Locate every blood parasite and identify its species.
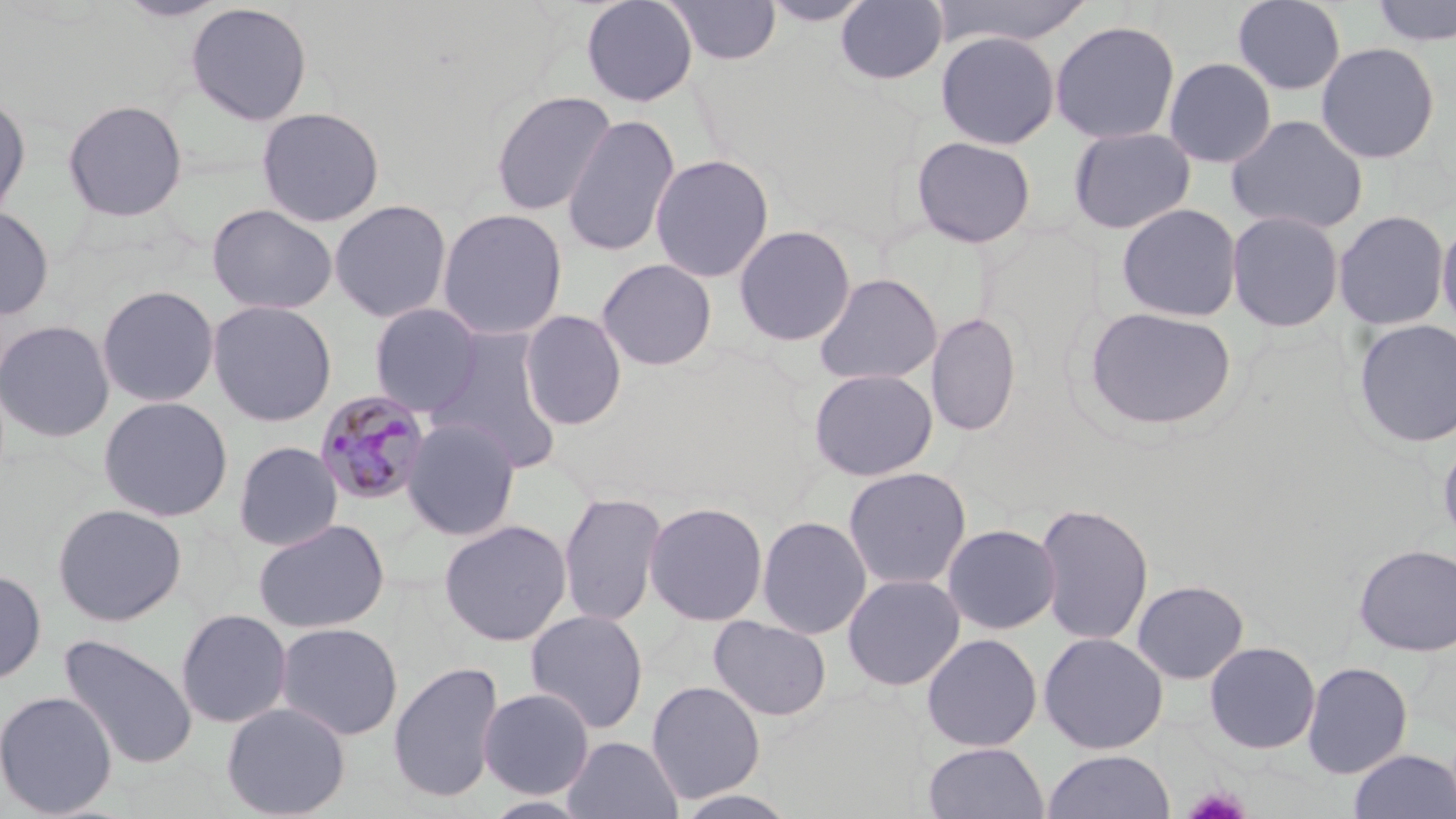

Approximate bounding boxes as [x1, y1, x2, y2] in pixels.
Plasmodium malariae-infected red blood cells: [314, 389, 432, 508].
No Plasmodium falciparum, Plasmodium ovale, Plasmodium vivax, Babesia divergens, or Trypanosoma brucei observed.

slide_level_diagnosis: Plasmodium malariae
field_of_view: single
stain: May-Grünwald-Giemsa
modality: light microscopy
magnification: 1000x
platelet_locations: 'approximate bounding boxes as [x1, y1, x2, y2] in pixels: [1181, 786, 1252, 818]'
preparation: thin blood smear
uninfected_red_blood_cell_locations: 'approximate bounding boxes as [x1, y1, x2, y2] in pixels: [117, 0, 230, 23], [580, 0, 699, 107], [664, 0, 782, 65], [760, 0, 874, 27], [835, 0, 948, 86], [929, 0, 1094, 48], [1231, 0, 1347, 95], [1369, 0, 1456, 46], [184, 2, 313, 126], [1049, 20, 1181, 144], [935, 30, 1060, 150], [1316, 41, 1441, 164], [1163, 56, 1277, 168], [490, 90, 616, 217], [0, 92, 31, 224], [62, 98, 188, 222], [256, 106, 386, 227], [561, 113, 681, 259], [1226, 113, 1369, 235], [1067, 126, 1196, 234], [911, 135, 1037, 249], [649, 153, 775, 283], [329, 199, 453, 323], [206, 203, 338, 316], [1116, 203, 1243, 322], [0, 205, 55, 321], [436, 207, 568, 340], [1226, 209, 1345, 332], [1333, 209, 1450, 331], [1436, 215, 1456, 335], [733, 224, 856, 347], [596, 258, 718, 371], [814, 272, 943, 386], [96, 284, 220, 408], [206, 299, 338, 427], [368, 302, 484, 416], [1081, 305, 1239, 434], [519, 309, 627, 430], [926, 311, 1022, 436], [1352, 318, 1456, 449], [0, 319, 116, 443], [427, 328, 564, 473], [808, 367, 938, 482], [97, 396, 233, 522], [402, 418, 520, 541], [1437, 434, 1456, 552], [233, 441, 343, 551], [842, 466, 972, 591], [558, 491, 667, 627], [644, 500, 769, 626], [1034, 501, 1155, 647], [51, 502, 188, 627], [756, 515, 872, 639], [252, 518, 391, 634], [438, 518, 573, 647], [941, 523, 1062, 635], [1353, 543, 1456, 657], [0, 568, 47, 685], [842, 573, 966, 691], [1131, 579, 1249, 684], [175, 608, 293, 728], [525, 609, 649, 734], [709, 615, 832, 721], [275, 622, 403, 741], [921, 632, 1043, 752], [1038, 632, 1168, 754], [59, 634, 197, 769], [1203, 640, 1321, 754], [388, 660, 504, 804], [1302, 660, 1413, 779], [646, 680, 766, 803], [478, 687, 595, 799], [0, 690, 117, 818], [221, 701, 351, 819], [562, 735, 683, 819], [923, 741, 1049, 819], [1041, 749, 1175, 819], [1348, 749, 1455, 818], [673, 789, 802, 818], [480, 794, 596, 818]'
image_size: 1456×819 pixels